Describe the morphology of the red blood cells.
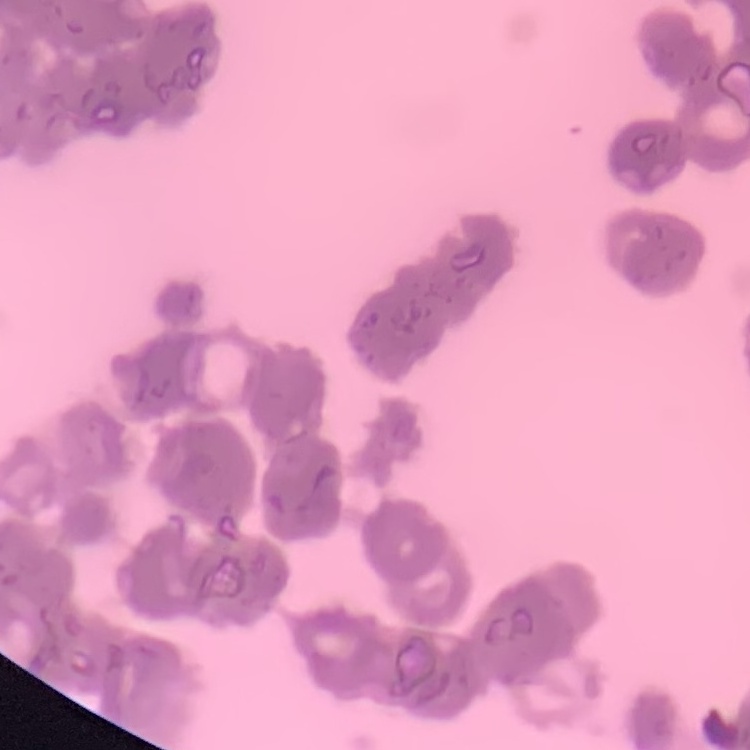

Rouleaux formation.

Summary:
  - Preparation: thin blood smear
  - Image type: square crop of a larger photomicrograph
  - Stain: Field's or Giemsa